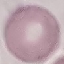

malaria_status: uninfected
image_type: automatically extracted cell patch, resized to 64 × 64 pixels
capture: smartphone through the microscope eyepiece
stain: Giemsa
preparation: thin smear